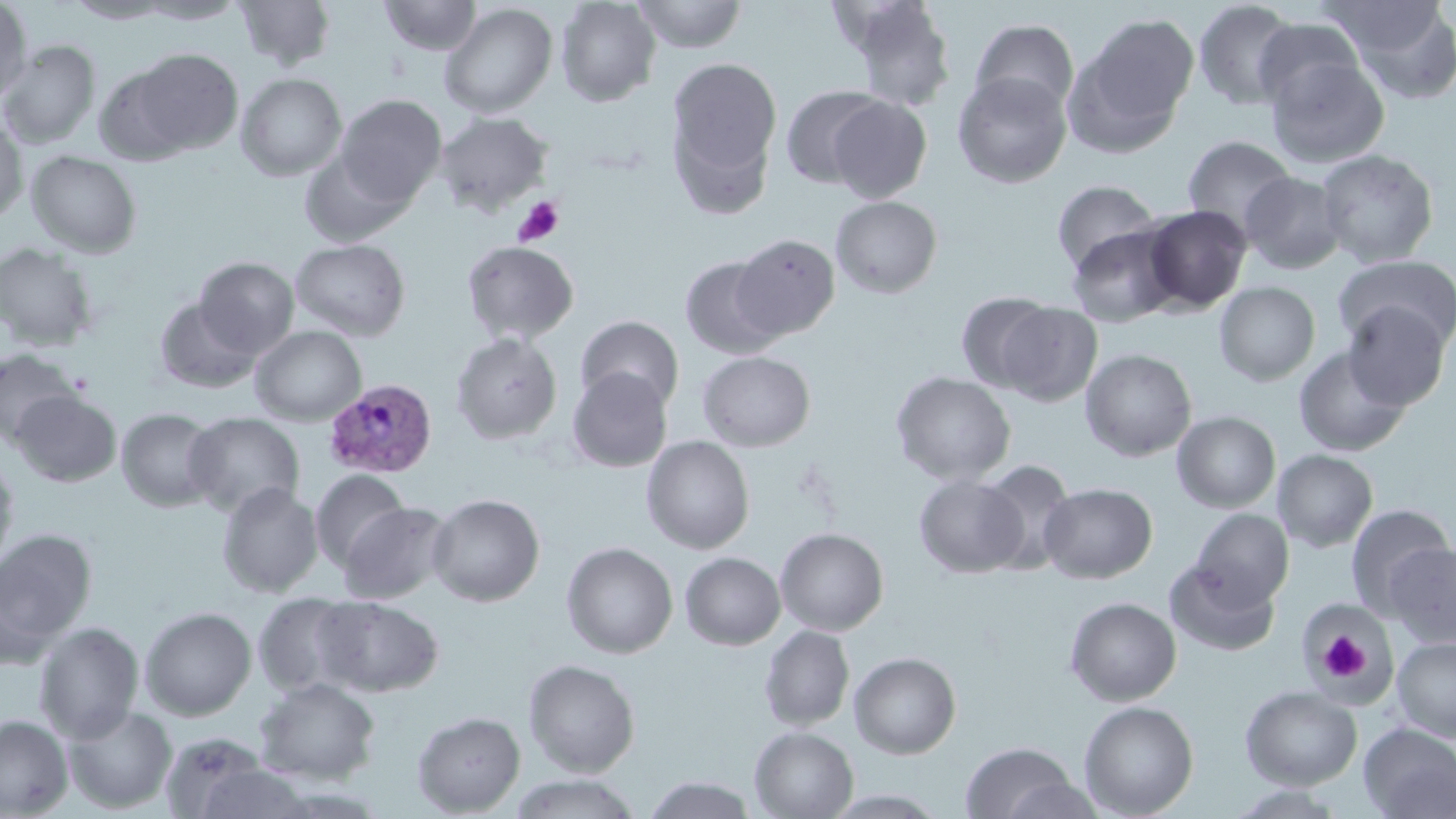
Approximate bounding boxes as named x1/y1/x2/y2 corners in pixels. Platelet locations: (x1=512, y1=196, x2=565, y2=247), (x1=1316, y1=627, x2=1371, y2=685). Uninfected red blood cell locations: (x1=64, y1=0, x2=175, y2=24), (x1=133, y1=0, x2=246, y2=24), (x1=235, y1=0, x2=335, y2=70), (x1=379, y1=0, x2=482, y2=56), (x1=631, y1=0, x2=748, y2=53), (x1=837, y1=0, x2=957, y2=111), (x1=0, y1=1, x2=32, y2=104), (x1=556, y1=1, x2=661, y2=107), (x1=1193, y1=1, x2=1299, y2=111), (x1=439, y1=3, x2=558, y2=119), (x1=1341, y1=3, x2=1456, y2=103), (x1=1077, y1=13, x2=1199, y2=140), (x1=1252, y1=17, x2=1366, y2=114), (x1=970, y1=19, x2=1079, y2=117), (x1=0, y1=41, x2=101, y2=148), (x1=131, y1=48, x2=243, y2=154), (x1=1265, y1=53, x2=1390, y2=169), (x1=666, y1=57, x2=782, y2=193), (x1=94, y1=66, x2=196, y2=165), (x1=952, y1=71, x2=1071, y2=188), (x1=236, y1=73, x2=347, y2=181), (x1=780, y1=85, x2=887, y2=188), (x1=336, y1=95, x2=447, y2=205), (x1=827, y1=97, x2=931, y2=203), (x1=434, y1=112, x2=552, y2=216), (x1=0, y1=116, x2=28, y2=225), (x1=1182, y1=135, x2=1297, y2=238), (x1=299, y1=147, x2=412, y2=247), (x1=25, y1=149, x2=143, y2=258), (x1=1315, y1=149, x2=1439, y2=268), (x1=1240, y1=171, x2=1347, y2=274), (x1=1052, y1=180, x2=1159, y2=275), (x1=830, y1=196, x2=942, y2=298), (x1=1142, y1=205, x2=1252, y2=313), (x1=1065, y1=224, x2=1181, y2=327), (x1=731, y1=233, x2=840, y2=340), (x1=290, y1=238, x2=411, y2=340), (x1=461, y1=240, x2=580, y2=344), (x1=0, y1=241, x2=100, y2=351), (x1=1334, y1=254, x2=1456, y2=353), (x1=679, y1=256, x2=787, y2=360), (x1=194, y1=257, x2=300, y2=357), (x1=1214, y1=281, x2=1320, y2=386), (x1=955, y1=291, x2=1058, y2=393), (x1=153, y1=298, x2=261, y2=393), (x1=997, y1=302, x2=1104, y2=406), (x1=1342, y1=302, x2=1451, y2=410), (x1=575, y1=315, x2=685, y2=412), (x1=249, y1=326, x2=366, y2=426), (x1=451, y1=332, x2=563, y2=444), (x1=1293, y1=346, x2=1413, y2=457), (x1=0, y1=348, x2=82, y2=446), (x1=1080, y1=349, x2=1197, y2=461), (x1=697, y1=351, x2=816, y2=452), (x1=567, y1=367, x2=673, y2=472), (x1=890, y1=371, x2=1016, y2=485), (x1=10, y1=389, x2=122, y2=486), (x1=116, y1=408, x2=221, y2=511), (x1=1172, y1=411, x2=1281, y2=513), (x1=184, y1=412, x2=304, y2=517), (x1=641, y1=435, x2=755, y2=554), (x1=1272, y1=449, x2=1378, y2=552), (x1=0, y1=452, x2=19, y2=572), (x1=977, y1=460, x2=1077, y2=575), (x1=310, y1=469, x2=409, y2=571), (x1=913, y1=473, x2=1027, y2=579), (x1=217, y1=482, x2=323, y2=598), (x1=1039, y1=482, x2=1157, y2=583), (x1=426, y1=493, x2=545, y2=607), (x1=339, y1=501, x2=453, y2=603), (x1=1345, y1=504, x2=1454, y2=616), (x1=1191, y1=509, x2=1294, y2=607), (x1=0, y1=528, x2=98, y2=657), (x1=775, y1=528, x2=889, y2=636), (x1=561, y1=542, x2=678, y2=659), (x1=1385, y1=543, x2=1455, y2=648), (x1=680, y1=552, x2=786, y2=650), (x1=1164, y1=559, x2=1282, y2=657), (x1=252, y1=593, x2=361, y2=697), (x1=314, y1=595, x2=444, y2=697), (x1=1064, y1=596, x2=1182, y2=706), (x1=140, y1=606, x2=257, y2=720), (x1=1305, y1=606, x2=1391, y2=696), (x1=34, y1=622, x2=144, y2=743), (x1=759, y1=625, x2=855, y2=731), (x1=1391, y1=636, x2=1456, y2=743), (x1=849, y1=651, x2=961, y2=759), (x1=523, y1=658, x2=640, y2=777), (x1=254, y1=677, x2=381, y2=785), (x1=1240, y1=686, x2=1362, y2=789), (x1=1079, y1=700, x2=1199, y2=818), (x1=62, y1=703, x2=177, y2=814), (x1=412, y1=711, x2=525, y2=816), (x1=0, y1=715, x2=73, y2=818), (x1=1358, y1=723, x2=1456, y2=819), (x1=749, y1=726, x2=858, y2=818), (x1=159, y1=732, x2=278, y2=819), (x1=960, y1=742, x2=1079, y2=819), (x1=509, y1=773, x2=642, y2=818), (x1=642, y1=775, x2=758, y2=818), (x1=1226, y1=785, x2=1351, y2=818), (x1=822, y1=789, x2=949, y2=817). Plasmodium vivax-infected red blood cell locations: (x1=324, y1=379, x2=438, y2=478). Slide-level diagnosis: Plasmodium vivax. Captured at 1000x magnification. May-Grünwald-Giemsa-stained preparation. Image is 1456×819 pixels. Optical microscopy. Thin blood film. Single field of view.